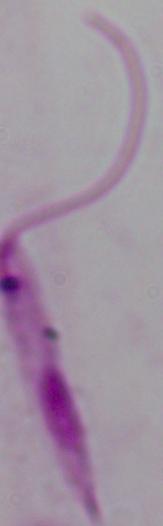
Summary:
  - Identification: Leishmania
  - Magnification: 1000x
  - Modality: micrograph